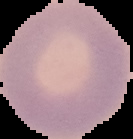
Image is 133×139 pixels. From a thin blood film. Result: negative for Plasmodium parasites. Segmented cell region on a black background.